Assess this cell for malaria.
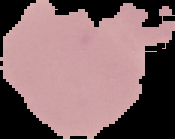
Uninfected.

Summary:
  - Image size: 175×139 pixels
  - Image type: segmented cell region on a black background
  - Preparation: thin blood smear